Classify this cell by malaria status.
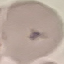
It is uninfected.

preparation = thin blood smear
stain = Giemsa
capture = smartphone camera at the microscope eyepiece
image type = cell patch, automatically extracted from a larger field of view and resized to 64 × 64 pixels